Name the cell type shown.
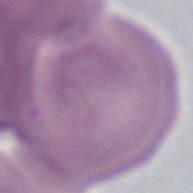

This is an erythrocyte.

Summary:
  - Modality: photomicrograph
  - Magnification: 1000x